State which parasite is depicted.
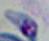

This is Toxoplasma gondii.

Summary:
  - Magnification: 1000x
  - Modality: micrograph